Draw a bounding box around every Plasmodium parasite, every leukocyte, and every artifact (stain precipitate or debris).
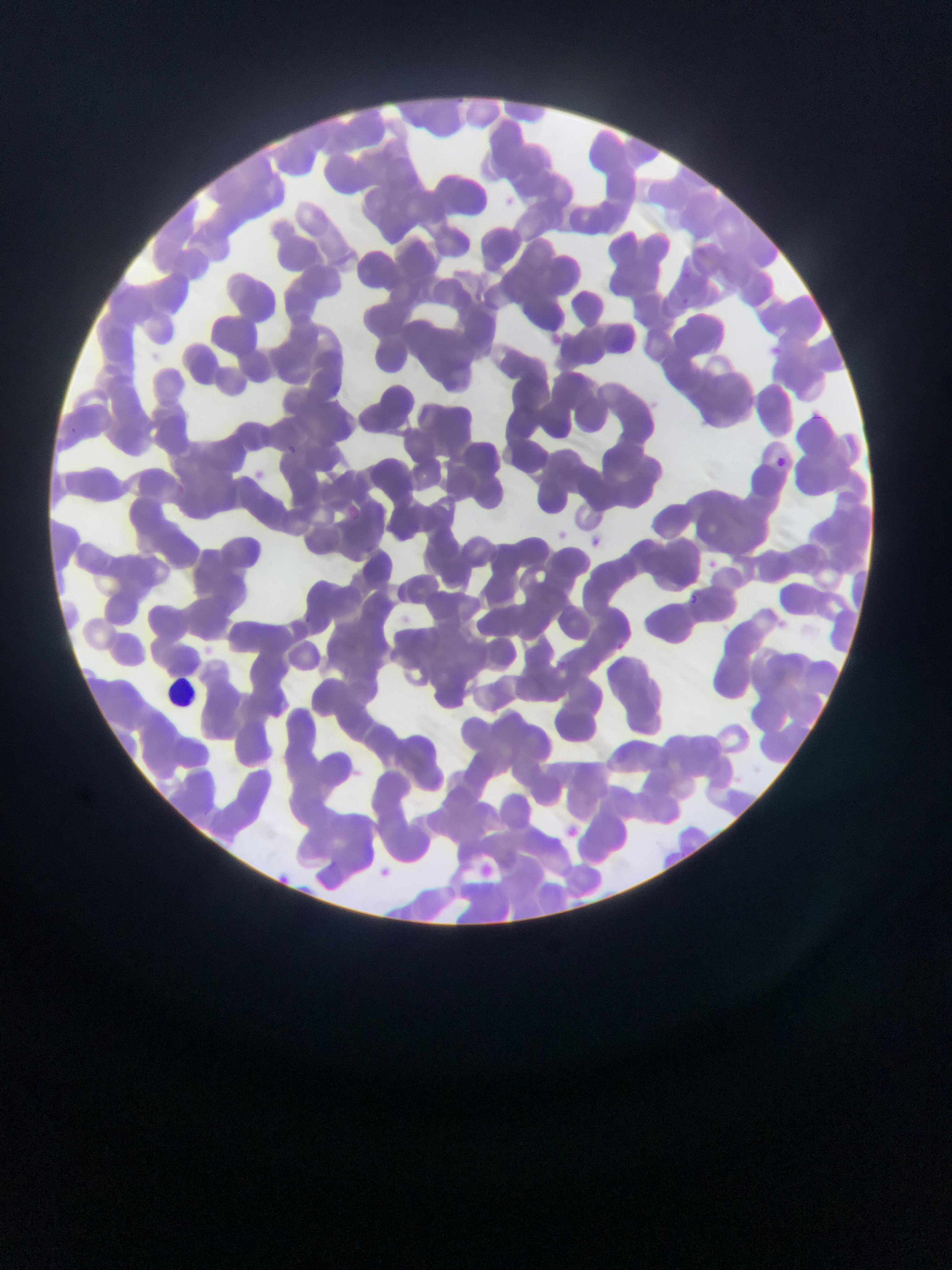
Approximate bounding boxes as [left, top, right, bottom] in pixels.
Plasmodium parasites: [490, 253, 503, 268], [286, 442, 297, 455], [776, 458, 786, 466], [348, 504, 360, 519], [688, 593, 699, 605], [303, 613, 310, 621].
Leukocytes: [162, 671, 203, 710].

Summary:
  - Field of view: single
  - Capture: mobile-phone photograph through a microscope
  - Country: Ghana
  - Image size: 952×1270 pixels
  - Preparation: thin blood smear